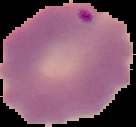

image size = 136×127 pixels
result = malaria parasites identified
preparation = thin blood film
image type = segmented cell region with the area outside set to black